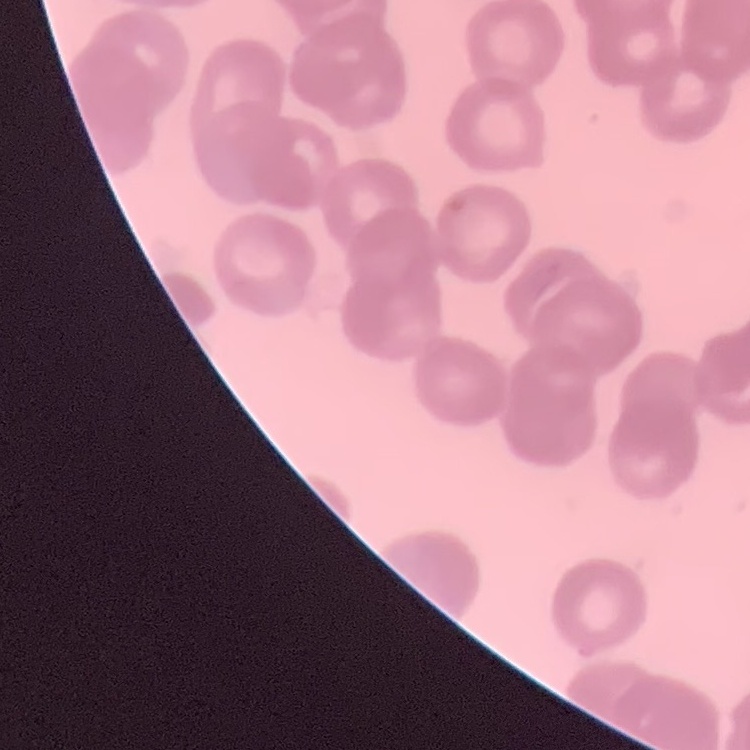 The red blood cells exhibit rouleaux formation. Thin blood smear. One tile cut from a larger photomicrograph. Stained with either Field's or Giemsa.